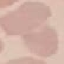

result = negative for malaria parasites
capture = smartphone camera at the microscope eyepiece
image type = automatically extracted cell patch, resized to 64 × 64 pixels
preparation = thin smear
stain = Giemsa